Assess this cell for malaria.
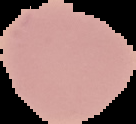

Uninfected.

{
  "preparation": "thin blood film",
  "image_type": "segmented cell region with the area outside set to black",
  "image_size": "136×124 pixels"
}